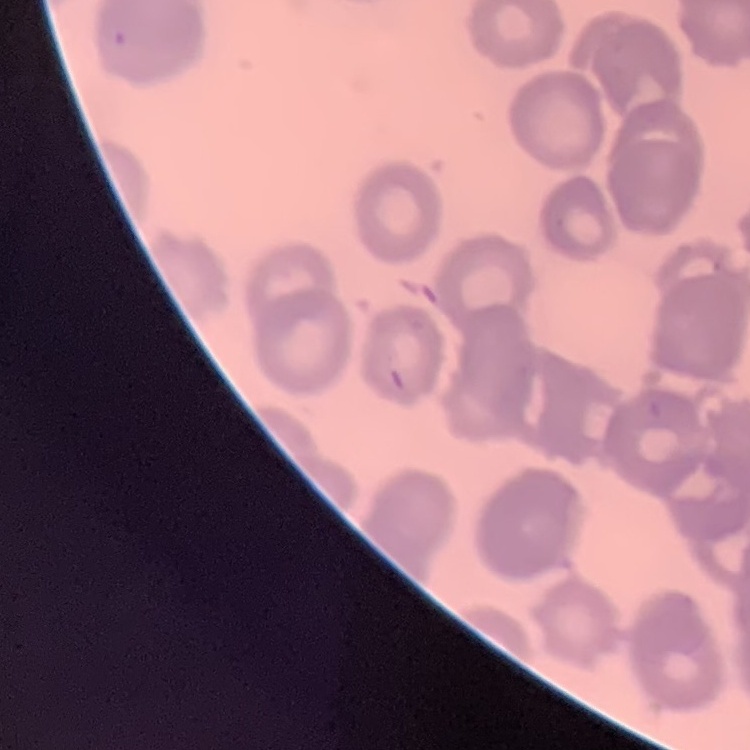
Summary:
  - Red blood cell morphology: rouleaux formation
  - Preparation: thin peripheral smear
  - Stain: Field's or Giemsa
  - Image type: one tile cut from a larger photomicrograph